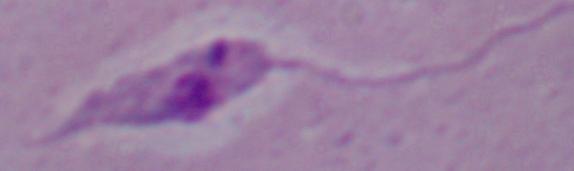

Micrograph. A Leishmania parasite is seen. Captured at 1000x magnification.